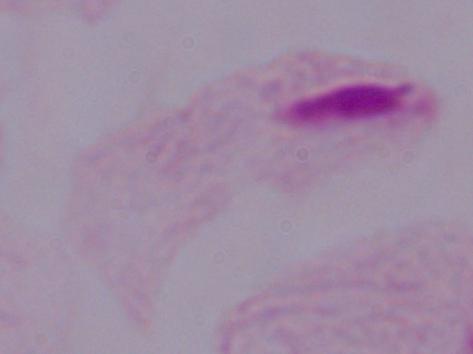

modality = micrograph
identification = trichomonad
magnification = 1000x